Describe the morphology of the erythrocytes.
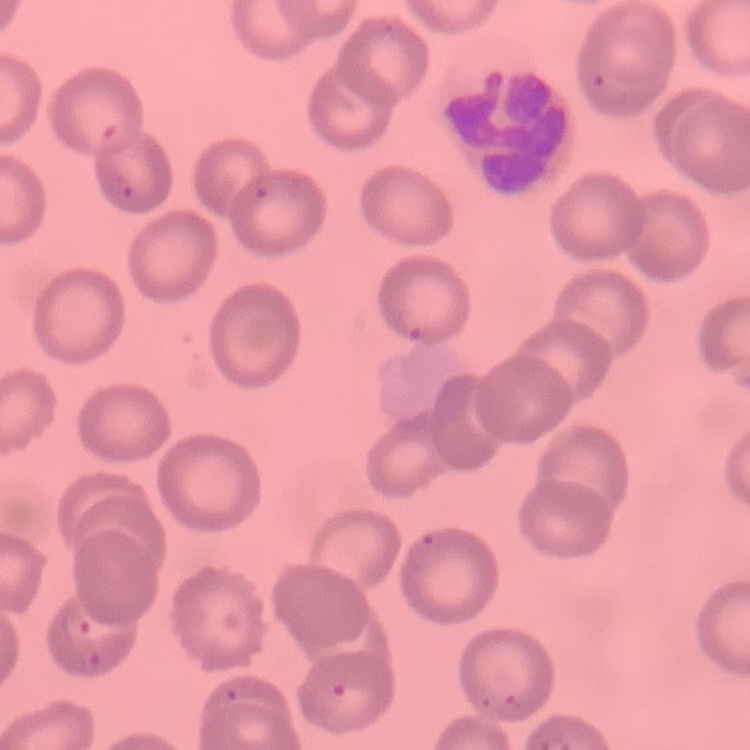

They show no rouleaux formation.

Thin blood film. One tile cut from a larger photomicrograph. Stained with either Field's or Giemsa.